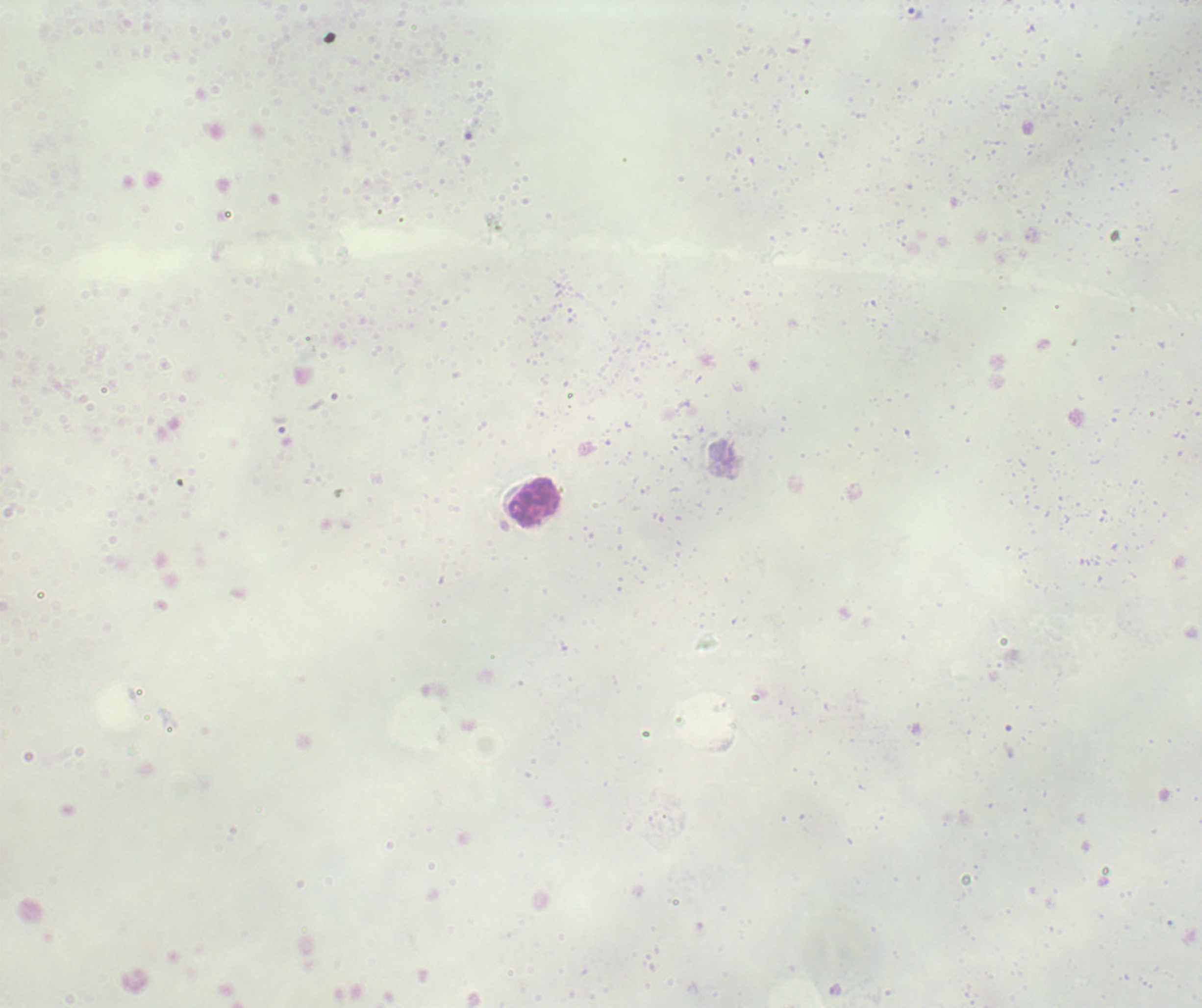

coordinate format = approximate object centers, in pixels from the top-left corner
leukocyte locations = (x=534, y=501)
trophozoite locations = (x=915, y=15)
stain = Romanowsky
magnification = 100x
field of view = single
context = previously used in a real diagnosis
coloration quality = bad
preparation = thick blood film
result = malaria parasites detected
image size = 1202×1008 pixels
background quality = unsatisfactory